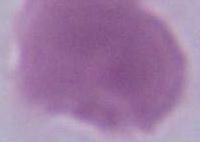
magnification = 1000x
modality = photomicrograph
identification = erythrocyte